Name the blood parasite species.
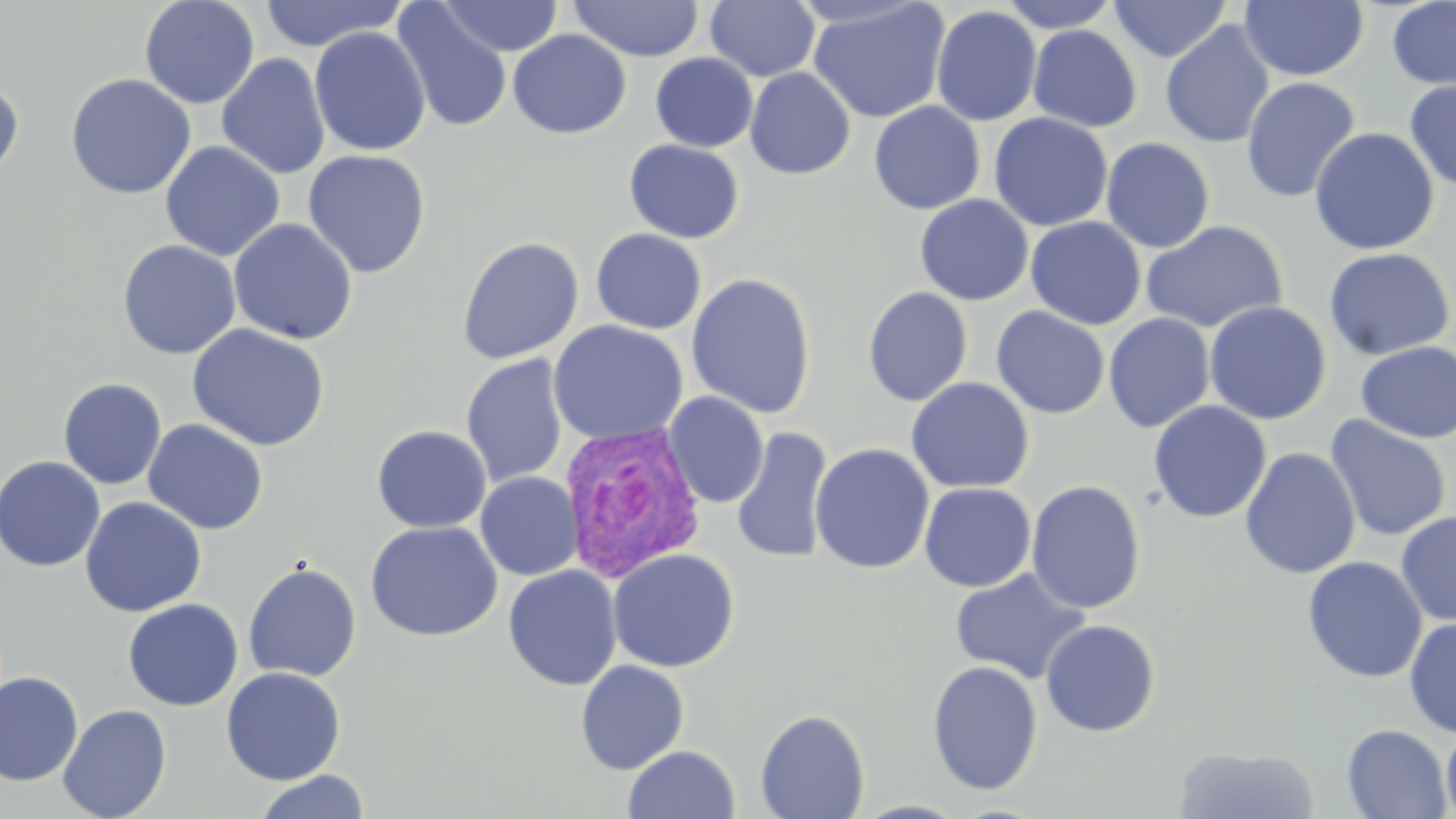
Plasmodium vivax.

{
  "magnification": "1000x",
  "preparation": "thin blood smear",
  "plasmodium_vivax_infected_red_blood_cell_locations": "approximate bounding boxes as [x1, y1, x2, y2] in pixels: [559, 420, 708, 583]",
  "stain": "May-Grünwald-Giemsa",
  "uninfected_red_blood_cell_locations": "approximate bounding boxes as [x1, y1, x2, y2] in pixels: [139, 0, 260, 109], [258, 0, 407, 51], [438, 0, 563, 57], [997, 0, 1122, 33], [1109, 0, 1232, 62], [567, 1, 704, 62], [705, 1, 820, 82], [808, 1, 950, 123], [1238, 1, 1369, 81], [1387, 1, 1456, 90], [391, 2, 512, 134], [931, 6, 1042, 127], [1160, 19, 1275, 149], [1028, 25, 1142, 132], [309, 26, 431, 157], [507, 29, 631, 140], [216, 53, 330, 179], [650, 53, 758, 152], [744, 68, 856, 180], [65, 73, 196, 200], [1240, 76, 1361, 204], [0, 77, 24, 186], [1403, 79, 1456, 193], [868, 101, 985, 214], [988, 112, 1114, 231], [1309, 126, 1439, 255], [1100, 137, 1215, 253], [624, 139, 744, 243], [160, 141, 285, 262], [302, 149, 431, 278], [914, 195, 1033, 306], [1025, 217, 1147, 330], [228, 218, 358, 345], [1140, 220, 1288, 334], [590, 228, 707, 334], [456, 236, 584, 365], [117, 239, 241, 359], [1322, 247, 1455, 360], [685, 273, 817, 418], [862, 287, 973, 406], [1204, 301, 1332, 425], [991, 306, 1110, 419], [1104, 313, 1215, 433], [548, 320, 689, 445], [187, 324, 331, 451], [1355, 341, 1456, 443], [460, 354, 570, 488], [57, 377, 167, 490], [906, 377, 1035, 493], [663, 391, 769, 508], [1148, 400, 1271, 523], [1324, 415, 1452, 542], [142, 419, 269, 535], [371, 425, 491, 533], [731, 425, 834, 565], [810, 443, 934, 574], [1239, 447, 1360, 580], [0, 455, 106, 572], [475, 472, 583, 580], [1026, 480, 1147, 614], [919, 483, 1036, 592], [80, 497, 207, 617], [1396, 510, 1456, 627], [365, 521, 503, 642], [607, 549, 741, 672], [1302, 556, 1427, 683], [242, 562, 363, 682], [503, 565, 622, 691], [950, 566, 1091, 684], [122, 598, 244, 711], [1404, 618, 1456, 738], [1039, 619, 1161, 738], [575, 660, 689, 775], [926, 660, 1044, 796], [221, 667, 346, 785], [0, 671, 84, 786], [57, 704, 172, 818], [755, 709, 870, 819], [1440, 721, 1456, 819], [1341, 724, 1453, 818], [622, 745, 740, 818], [1172, 746, 1320, 819], [253, 770, 370, 819]",
  "field_of_view": "one of a larger specimen",
  "image_size": "1456×819 pixels",
  "modality": "optical microscopy"
}